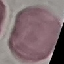

result = no malaria parasites detected
preparation = thin blood film
stain = Giemsa
image type = cell patch, automatically extracted from a larger field of view and resized to 64 × 64 pixels
capture = smartphone camera at the microscope eyepiece